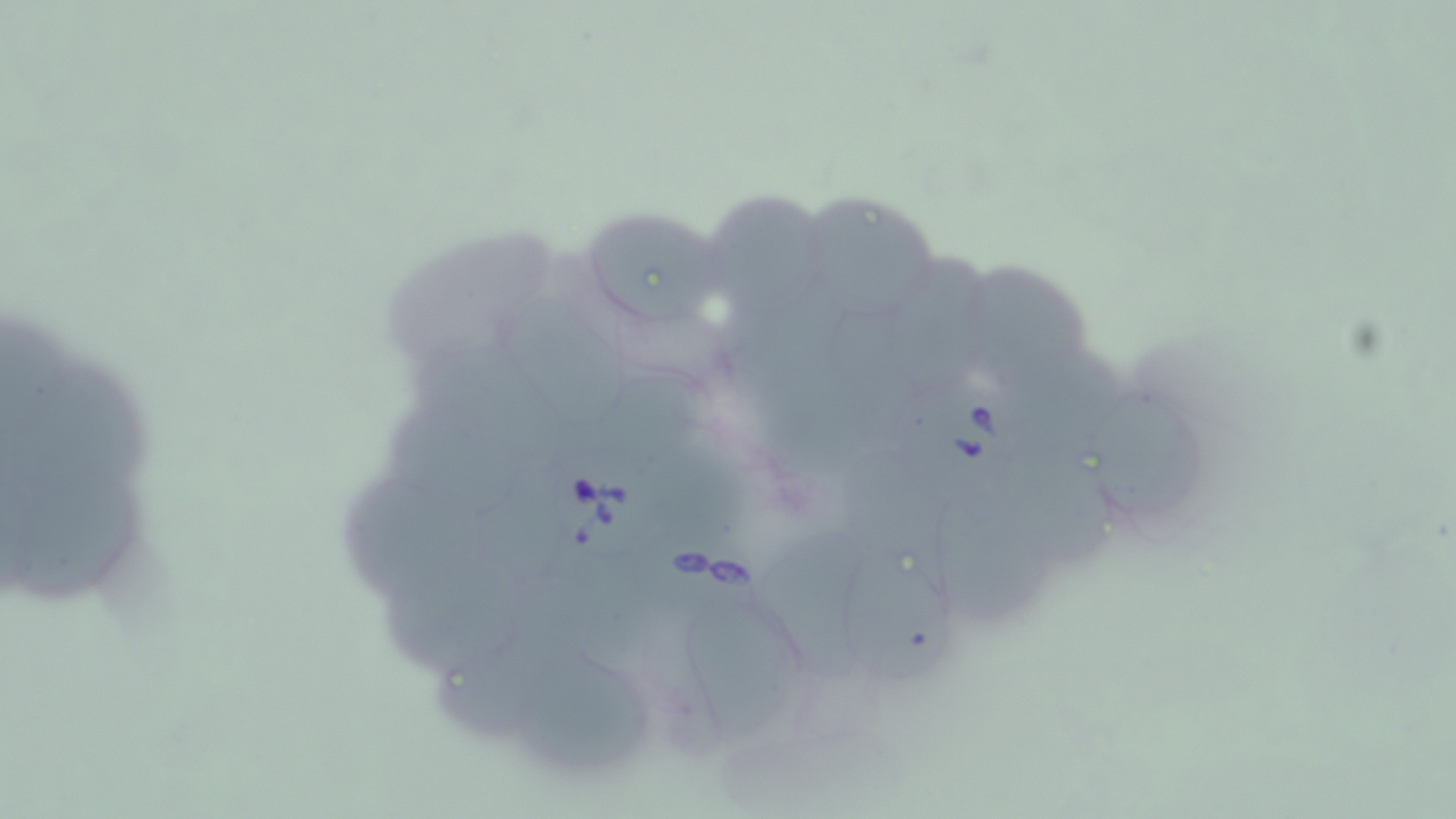

Summary:
  - Coordinate format: approximate bounding boxes as [x1, y1, x2, y2] in pixels
  - Uninfected red blood cell locations: [708, 193, 825, 314], [797, 197, 943, 315], [589, 215, 722, 328], [895, 250, 992, 385], [965, 266, 1092, 388], [730, 281, 850, 402], [500, 299, 626, 421], [1020, 351, 1119, 474], [23, 358, 158, 501], [589, 371, 702, 462], [1092, 388, 1210, 521], [383, 411, 525, 516], [840, 449, 947, 585], [1011, 460, 1113, 563], [16, 471, 150, 609], [344, 480, 484, 584], [934, 500, 1049, 628], [757, 535, 874, 687], [393, 550, 528, 672], [841, 553, 959, 685], [683, 600, 808, 743], [437, 613, 570, 733], [518, 650, 653, 768]
  - Babesia divergens-infected red blood cell locations: [909, 377, 1041, 504], [556, 449, 678, 562], [634, 517, 774, 627]
  - Slide-level diagnosis: Babesia divergens
  - Image size: 1456×819 pixels
  - Field of view: single
  - Stain: May-Grünwald-Giemsa
  - Magnification: 1000x
  - Preparation: thin blood smear
  - Modality: optical microscopy